Assess this cell for malaria.
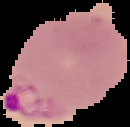
Parasitized.

Summary:
  - Image type: segmented cell region on a black background
  - Preparation: thin blood smear
  - Image size: 130×127 pixels